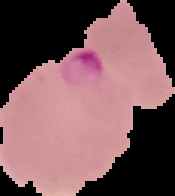
image size = 175×196 pixels
image type = segmented cell region with the area outside set to black
preparation = thin blood film
result = malaria parasites identified